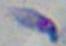 Captured at 1000x magnification. Photomicrograph. Toxoplasma gondii is seen.